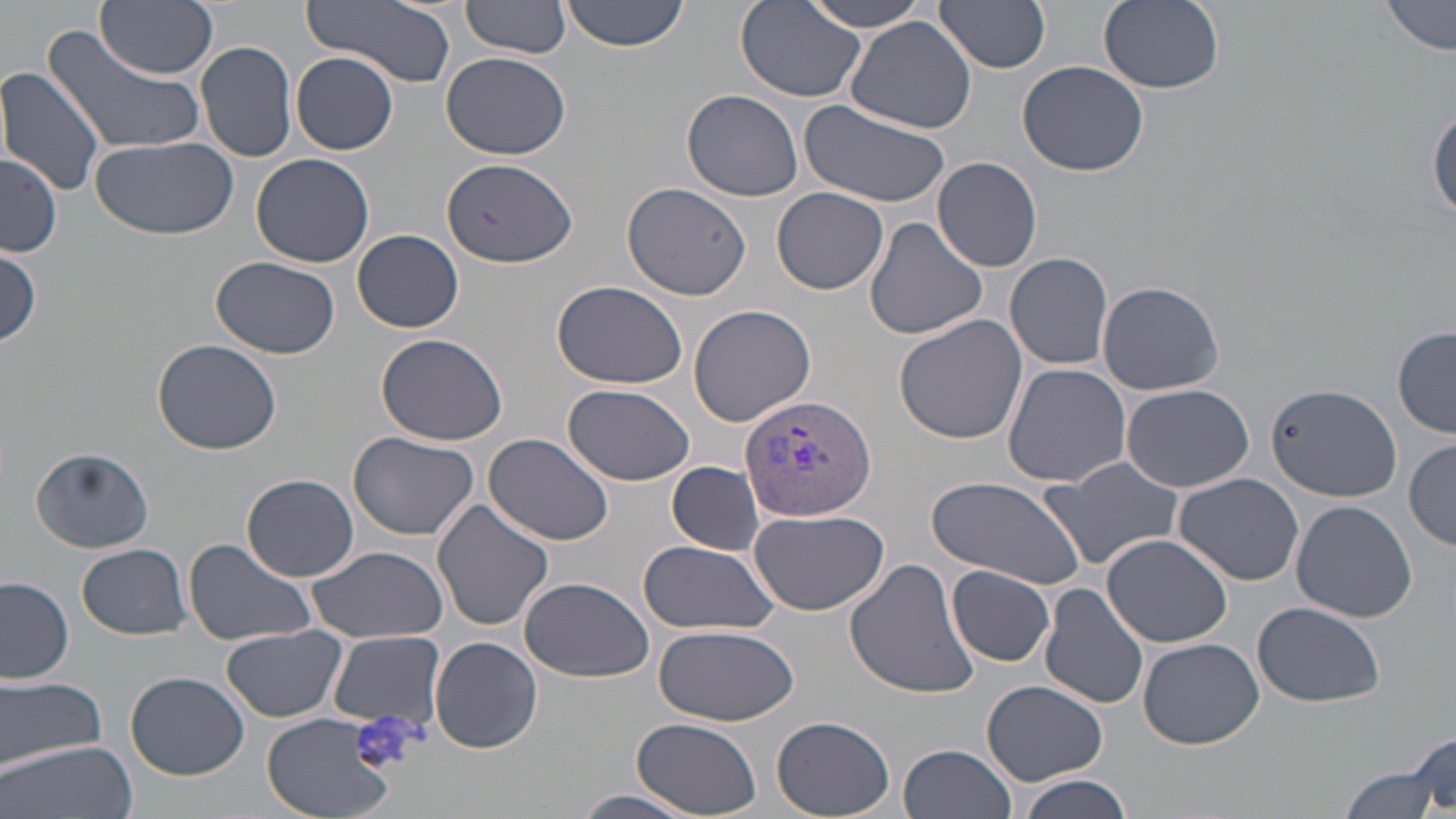

Summary:
  - Coordinate format: approximate bounding boxes as named x1/y1/x2/y2 corners in pixels
  - Platelet locations: (x1=351, y1=711, x2=419, y2=774)
  - Plasmodium vivax-infected red blood cell locations: (x1=738, y1=395, x2=878, y2=521)
  - Uninfected red blood cell locations: (x1=97, y1=0, x2=217, y2=77), (x1=301, y1=0, x2=458, y2=90), (x1=562, y1=0, x2=694, y2=51), (x1=800, y1=0, x2=935, y2=32), (x1=935, y1=0, x2=1052, y2=73), (x1=1383, y1=0, x2=1454, y2=57), (x1=460, y1=1, x2=572, y2=63), (x1=1098, y1=1, x2=1224, y2=94), (x1=737, y1=4, x2=868, y2=103), (x1=844, y1=15, x2=978, y2=133), (x1=42, y1=22, x2=211, y2=156), (x1=196, y1=39, x2=298, y2=164), (x1=441, y1=52, x2=571, y2=161), (x1=291, y1=53, x2=399, y2=154), (x1=1017, y1=61, x2=1150, y2=176), (x1=0, y1=66, x2=106, y2=196), (x1=680, y1=90, x2=804, y2=202), (x1=802, y1=100, x2=951, y2=208), (x1=1429, y1=106, x2=1456, y2=223), (x1=90, y1=135, x2=238, y2=241), (x1=1, y1=151, x2=62, y2=257), (x1=251, y1=153, x2=374, y2=268), (x1=441, y1=157, x2=578, y2=271), (x1=934, y1=157, x2=1043, y2=272), (x1=622, y1=182, x2=752, y2=301), (x1=773, y1=187, x2=889, y2=294), (x1=864, y1=216, x2=988, y2=340), (x1=353, y1=229, x2=464, y2=333), (x1=1, y1=245, x2=41, y2=347), (x1=1005, y1=251, x2=1115, y2=370), (x1=212, y1=257, x2=339, y2=359), (x1=1095, y1=279, x2=1225, y2=395), (x1=551, y1=280, x2=689, y2=389), (x1=688, y1=302, x2=817, y2=427), (x1=893, y1=315, x2=1028, y2=444), (x1=1393, y1=327, x2=1455, y2=437), (x1=375, y1=332, x2=509, y2=446), (x1=152, y1=339, x2=281, y2=456), (x1=1002, y1=362, x2=1133, y2=487), (x1=1121, y1=383, x2=1254, y2=492), (x1=562, y1=384, x2=694, y2=486), (x1=1268, y1=384, x2=1400, y2=500), (x1=347, y1=431, x2=479, y2=539), (x1=484, y1=431, x2=618, y2=547), (x1=1406, y1=438, x2=1455, y2=550), (x1=32, y1=447, x2=154, y2=553), (x1=1036, y1=457, x2=1185, y2=572), (x1=666, y1=461, x2=764, y2=555), (x1=1173, y1=473, x2=1305, y2=587), (x1=243, y1=475, x2=361, y2=582), (x1=924, y1=475, x2=1087, y2=585), (x1=433, y1=499, x2=557, y2=631), (x1=1290, y1=500, x2=1418, y2=623), (x1=747, y1=507, x2=890, y2=616), (x1=1100, y1=534, x2=1233, y2=647), (x1=182, y1=537, x2=318, y2=647), (x1=639, y1=540, x2=777, y2=636), (x1=77, y1=545, x2=192, y2=640), (x1=306, y1=546, x2=448, y2=643), (x1=845, y1=557, x2=979, y2=698), (x1=947, y1=566, x2=1056, y2=667), (x1=0, y1=576, x2=74, y2=682), (x1=519, y1=576, x2=656, y2=683), (x1=1040, y1=583, x2=1150, y2=711), (x1=1252, y1=602, x2=1385, y2=707), (x1=654, y1=624, x2=800, y2=728), (x1=223, y1=626, x2=347, y2=722), (x1=328, y1=632, x2=446, y2=729), (x1=429, y1=637, x2=543, y2=753), (x1=1137, y1=637, x2=1263, y2=749), (x1=126, y1=671, x2=248, y2=779), (x1=0, y1=676, x2=107, y2=769), (x1=982, y1=679, x2=1108, y2=785), (x1=262, y1=712, x2=396, y2=819), (x1=771, y1=716, x2=895, y2=819), (x1=632, y1=719, x2=764, y2=817), (x1=1406, y1=733, x2=1455, y2=813), (x1=0, y1=741, x2=139, y2=819), (x1=899, y1=743, x2=1017, y2=819), (x1=1335, y1=759, x2=1447, y2=819), (x1=1014, y1=774, x2=1136, y2=819), (x1=565, y1=788, x2=711, y2=819)
  - Slide-level diagnosis: Plasmodium vivax
  - Preparation: thin blood film
  - Image size: 1456×819 pixels
  - Magnification: 1000x
  - Stain: May-Grünwald-Giemsa
  - Field of view: single
  - Modality: optical microscopy